Classify this cell by malaria status.
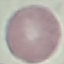
It is uninfected.

Summary:
  - Stain: Giemsa
  - Capture: smartphone through the microscope eyepiece
  - Image type: cell patch, automatically extracted from a larger field of view and resized to 64 × 64 pixels
  - Preparation: thin smear